Name the parasite shown.
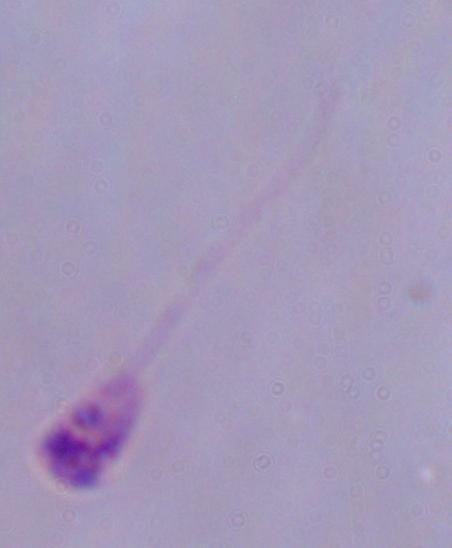
This is Leishmania.

Summary:
  - Magnification: 1000x
  - Modality: micrograph